Outline platelets.
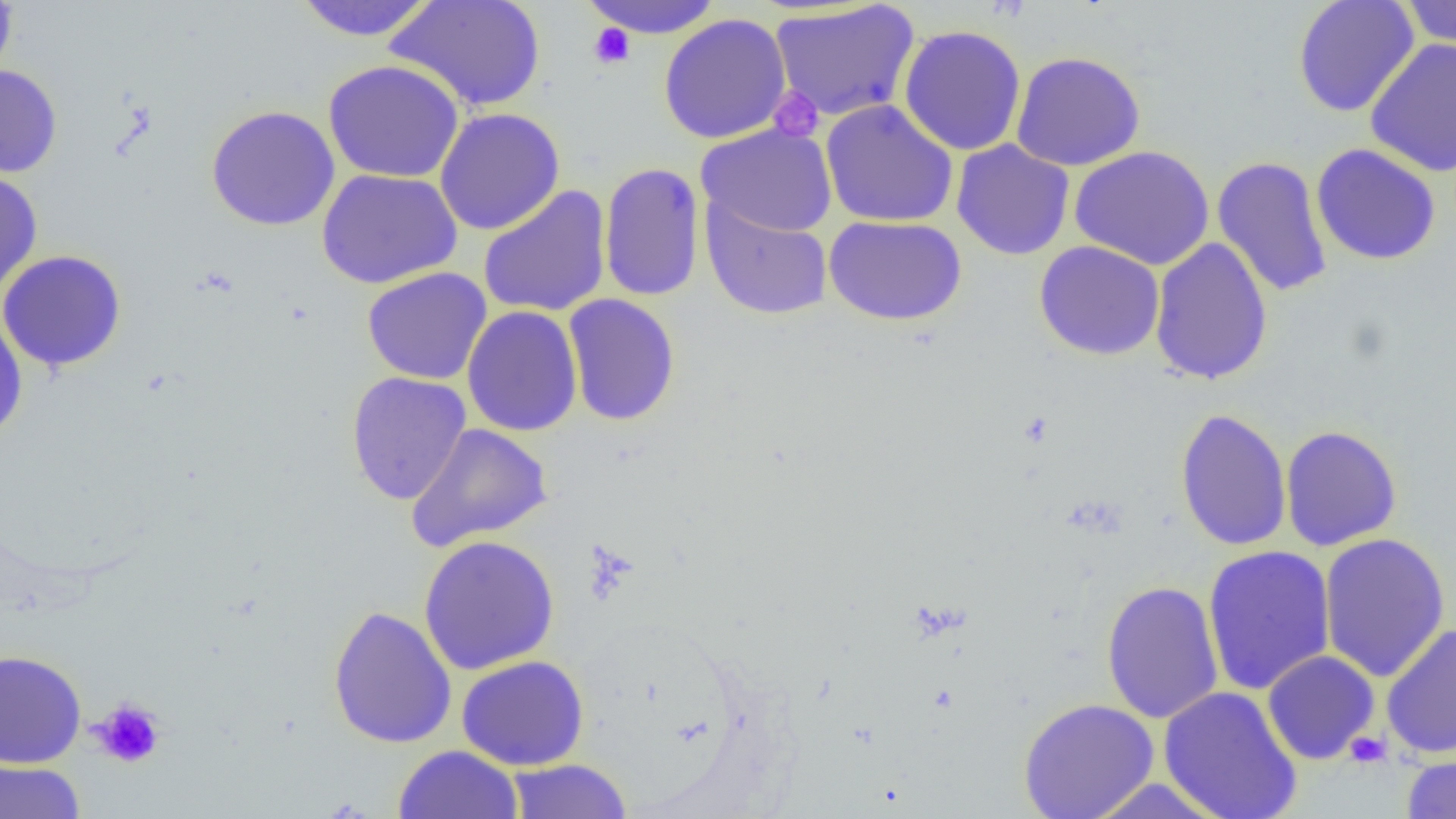

Approximate bounding boxes as (x1,y1)-(x2,y2) corner pairs in pixels.
Platelets: (588,23)-(635,69), (768,87)-(824,143), (90,697)-(166,769), (1344,731)-(1391,767).

Summary:
  - Uninfected red blood cell locations: (0,0)-(17,88), (385,0)-(547,113), (579,0)-(725,38), (1292,0)-(1420,118), (293,1)-(439,42), (1398,1)-(1456,49), (770,2)-(920,121), (659,13)-(791,144), (898,24)-(1027,156), (1365,38)-(1456,177), (1010,50)-(1146,171), (322,59)-(465,183), (0,64)-(63,178), (820,99)-(959,228), (205,104)-(341,231), (434,107)-(565,236), (696,123)-(838,237), (951,140)-(1075,260), (1311,143)-(1442,266), (1069,145)-(1214,270), (1212,156)-(1332,298), (586,160)-(692,428), (598,161)-(706,302), (0,168)-(43,299), (316,168)-(463,289), (477,185)-(612,318), (700,197)-(834,321), (824,215)-(967,326), (1149,237)-(1274,386), (1034,241)-(1165,361), (0,249)-(127,372), (361,267)-(492,385), (563,294)-(680,426), (462,306)-(583,437), (0,310)-(28,442), (345,371)-(471,505), (1175,407)-(1292,551), (404,422)-(553,553), (1280,424)-(1402,551), (1319,532)-(1451,682), (419,534)-(560,675), (1202,544)-(1336,696), (1100,580)-(1224,724), (328,604)-(457,749), (1381,623)-(1456,759), (0,649)-(87,768), (1262,650)-(1380,764), (456,655)-(589,770), (1158,685)-(1303,819), (1017,697)-(1160,819), (393,745)-(524,818), (1401,753)-(1456,818), (505,758)-(634,818), (0,760)-(86,819), (1086,778)-(1229,818)
  - Slide-level diagnosis: negative for blood parasites
  - Modality: light microscopy
  - Image size: 1456×819 pixels
  - Preparation: thin blood smear
  - Field of view: single
  - Magnification: 1000x